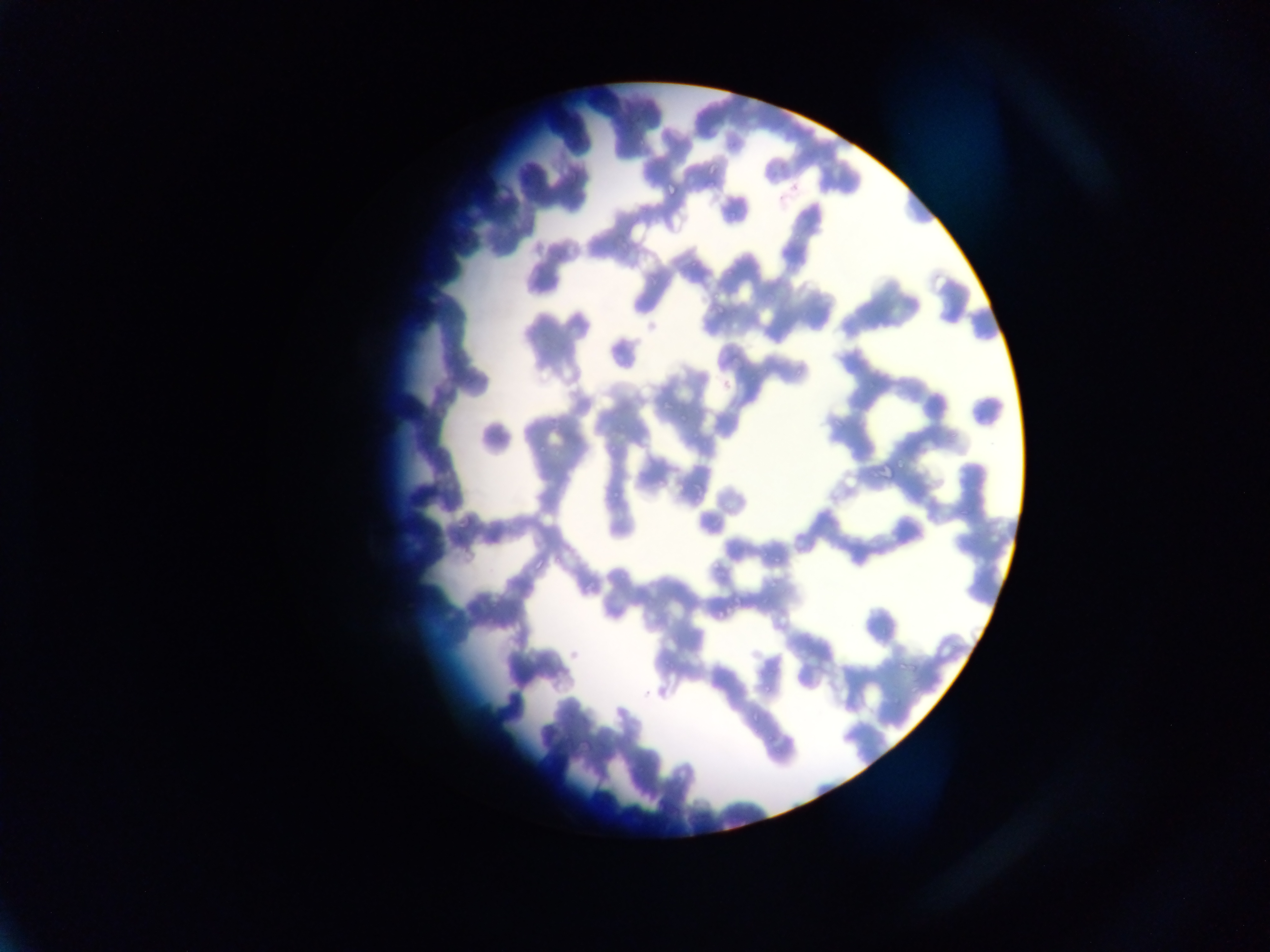

image size = 1270×952 pixels
field of view = single
country = Ghana
preparation = thin blood smear
Plasmodium parasite locations = approximate bounding boxes as left top right bottom in pixels: 689 259 699 270; 714 305 725 316; 761 681 772 691
capture = mobile-phone photograph through a microscope